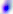
Summary:
  - Identification: Toxoplasma gondii
  - Modality: photomicrograph
  - Magnification: 400x